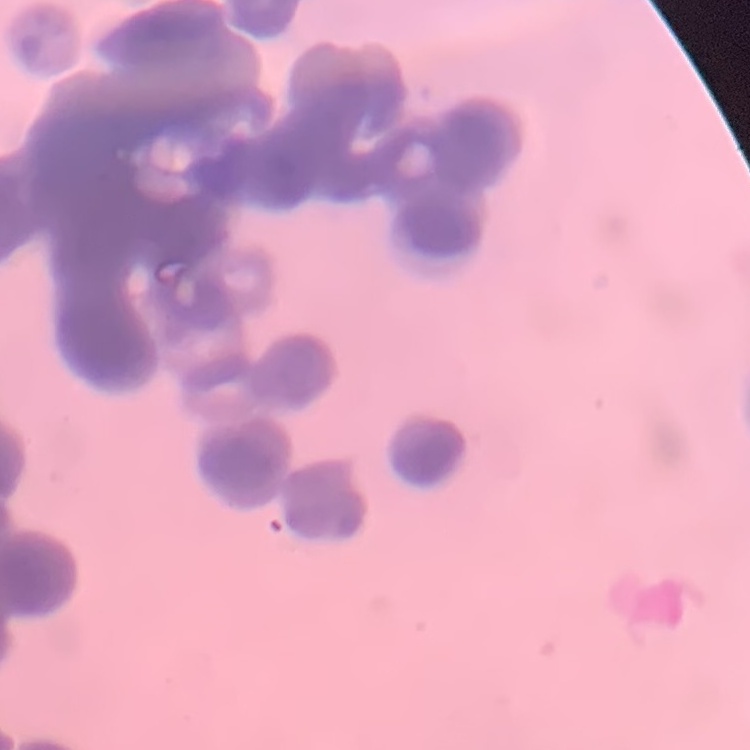

Summary:
  - Red blood cell morphology: rouleaux formation
  - Image type: one tile cut from a larger photomicrograph
  - Stain: Field's or Giemsa
  - Preparation: thin peripheral smear